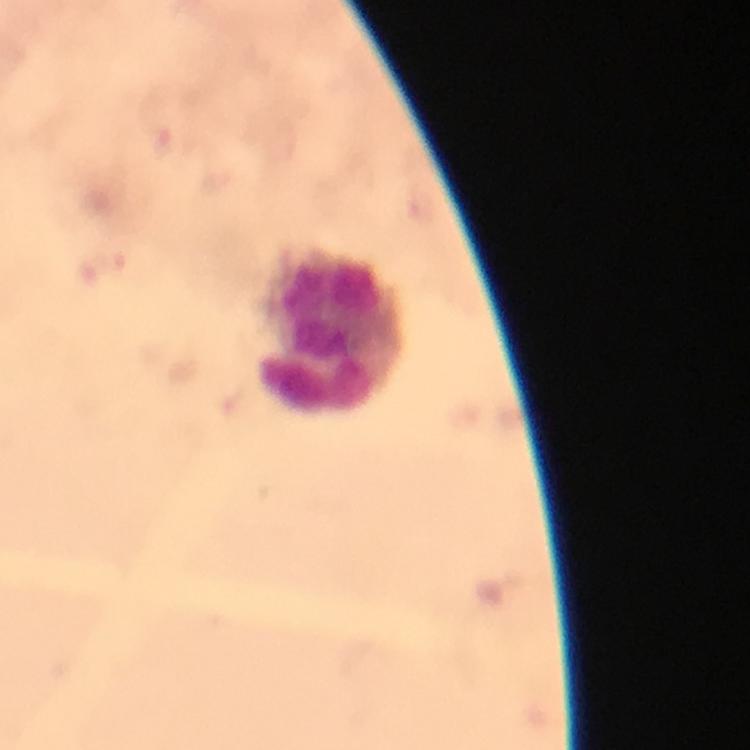
Approximate centers as (x, y) in pixels. Leukocyte locations: (334, 329). 100x magnification. Immersion oil was used. From a malaria diagnostic workup. Thick smear. Cropped region of a single field of view. Photographed with a smartphone mounted on the microscope. Giemsa-stained preparation. Malaria parasites: none seen. Image is 750×750 pixels.